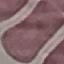
result = no malaria parasites seen
stain = Giemsa
image type = automatically extracted cell patch, resized to 64 × 64 pixels
preparation = thin smear
capture = smartphone through the microscope eyepiece